Assess for Plasmodium parasites.
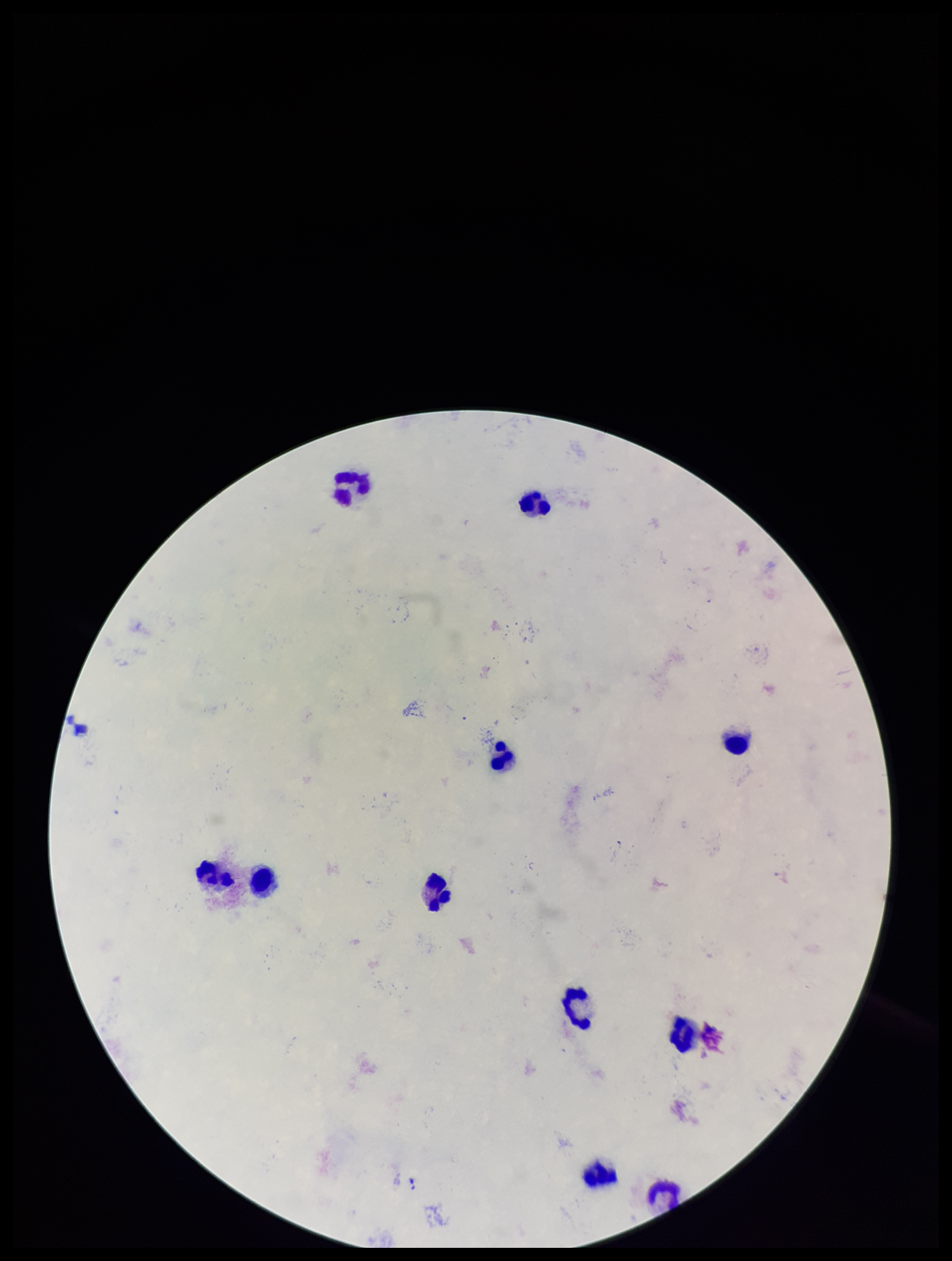
None detected.

{
  "parasite_count": 0,
  "capture": "smartphone photograph through the microscope eyepiece",
  "patient_malaria_status": "negative",
  "field_of_view": "one from this slide",
  "image_size": "952×1261 pixels",
  "leukocyte_count": 11,
  "preparation": "thick blood smear",
  "stain": "Giemsa"
}